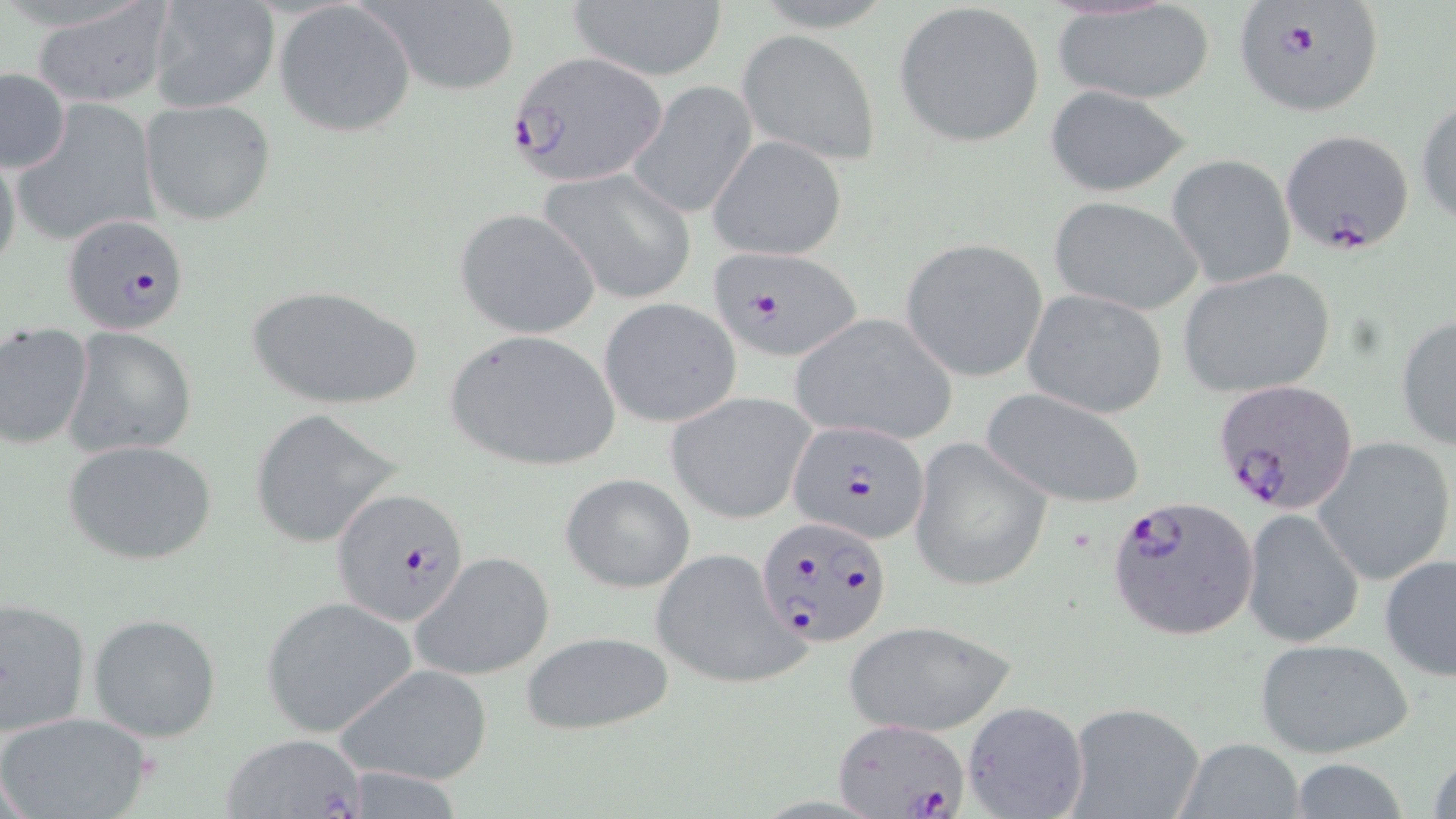
Summary:
  - Coordinate format: approximate bounding boxes as (x1, y1, x2, y2) in pixels
  - Plasmodium falciparum-infected red blood cell locations: (1235, 5, 1384, 120), (508, 49, 669, 187), (1278, 129, 1414, 256), (63, 214, 190, 336), (711, 248, 864, 361), (1211, 379, 1360, 515), (787, 419, 933, 546), (332, 488, 470, 626), (1105, 493, 1260, 641), (754, 515, 891, 648), (831, 717, 971, 819)
  - Uninfected red blood cell locations: (148, 0, 280, 111), (561, 0, 731, 83), (365, 1, 522, 95), (27, 2, 178, 108), (893, 2, 1046, 148), (274, 3, 416, 136), (1052, 3, 1216, 106), (736, 29, 881, 167), (1, 69, 70, 173), (627, 80, 757, 220), (1044, 85, 1193, 198), (1415, 96, 1456, 227), (140, 100, 274, 225), (14, 102, 165, 245), (710, 137, 848, 258), (0, 147, 22, 280), (1165, 154, 1297, 288), (539, 169, 696, 304), (1046, 195, 1205, 315), (455, 209, 599, 339), (900, 238, 1048, 382), (1175, 267, 1337, 398), (244, 282, 424, 411), (1022, 290, 1170, 419), (598, 298, 741, 428), (789, 312, 959, 444), (1394, 314, 1456, 451), (0, 323, 94, 448), (64, 328, 196, 459), (444, 330, 624, 473), (980, 387, 1150, 510), (664, 391, 816, 524), (248, 408, 405, 550), (907, 436, 1052, 594), (1313, 437, 1455, 587), (62, 439, 218, 566), (560, 472, 695, 594), (1243, 507, 1365, 649), (650, 545, 807, 692), (409, 551, 556, 682), (1380, 554, 1456, 681), (1, 595, 92, 738), (260, 599, 417, 736), (86, 612, 224, 743), (841, 619, 1015, 737), (517, 630, 675, 736), (1252, 637, 1416, 758), (339, 663, 494, 785), (959, 699, 1089, 819), (1062, 702, 1205, 819), (0, 710, 157, 819), (219, 732, 370, 819), (1173, 737, 1310, 819), (1427, 742, 1456, 819), (1284, 759, 1415, 817)
  - Slide-level diagnosis: Plasmodium falciparum
  - Field of view: one of a larger specimen
  - Image size: 1456×819 pixels
  - Preparation: thin blood smear
  - Magnification: 1000x
  - Stain: May-Grünwald-Giemsa
  - Modality: optical microscopy